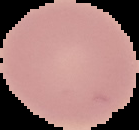

Image is 139×130 pixels. From a thin blood smear. Cell region segmented out of the field of view; the surrounding area is masked to black. Malaria status: uninfected.